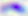

Photomicrograph. Toxoplasma gondii is shown. 400x magnification.